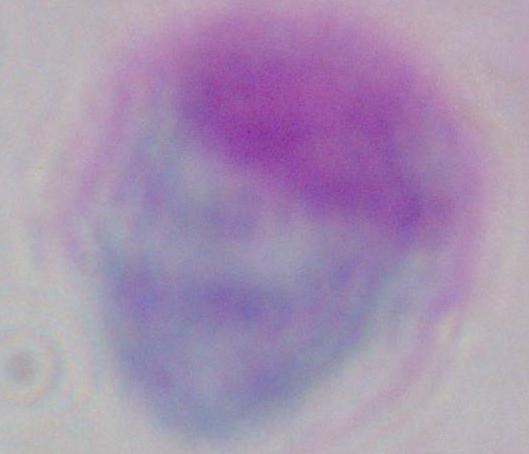

modality = photomicrograph
magnification = 1000x
identification = white blood cell